Locate every Plasmodium falciparum-infected red blood cell.
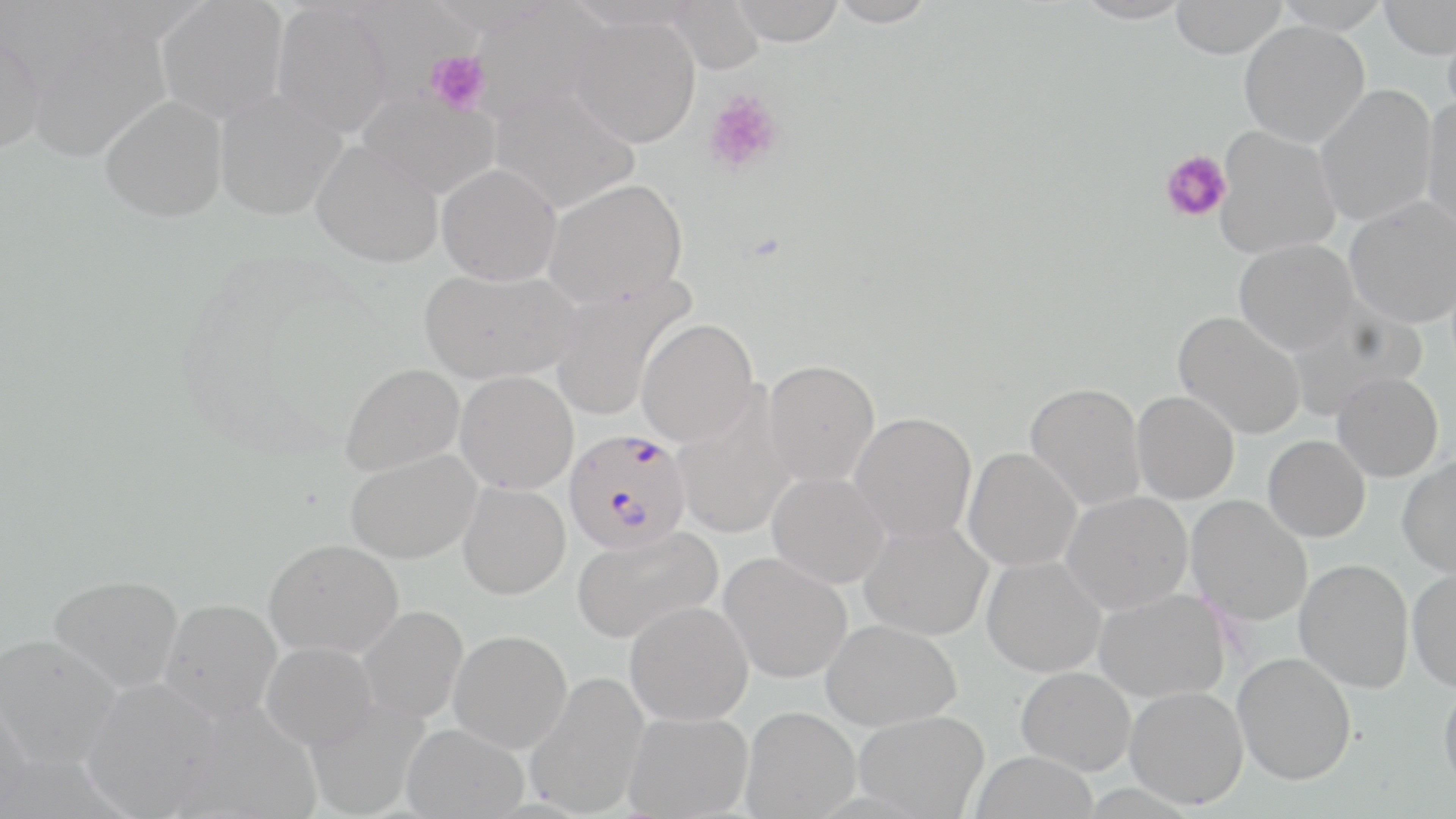

Approximate bounding boxes as (x1, y1, x2, y2) in pixels.
Plasmodium falciparum-infected red blood cells: (563, 428, 692, 553).

slide-level diagnosis = Plasmodium falciparum
preparation = thin blood film
stain = May-Grünwald-Giemsa
uninfected red blood cell locations = approximate bounding boxes as (x1, y1, x2, y2) in pixels: (156, 0, 289, 123), (666, 0, 765, 74), (728, 0, 845, 45), (826, 0, 939, 27), (1071, 0, 1194, 24), (1170, 0, 1288, 58), (1271, 0, 1392, 33), (1379, 1, 1456, 60), (271, 2, 394, 137), (469, 2, 607, 123), (568, 14, 701, 148), (1442, 14, 1456, 125), (24, 20, 170, 163), (1239, 21, 1370, 147), (0, 30, 46, 154), (1314, 85, 1438, 226), (489, 86, 641, 212), (213, 89, 346, 220), (357, 90, 500, 199), (99, 95, 227, 222), (1421, 98, 1456, 237), (1214, 126, 1341, 260), (311, 139, 443, 267), (436, 163, 563, 285), (543, 178, 688, 307), (1344, 197, 1456, 328), (1234, 238, 1359, 354), (419, 268, 579, 384), (550, 276, 695, 422), (1285, 299, 1427, 417), (1173, 311, 1306, 440), (636, 318, 758, 446), (763, 359, 880, 486), (340, 363, 464, 476), (455, 370, 579, 494), (1332, 371, 1443, 482), (1025, 382, 1146, 511), (671, 390, 796, 539), (1132, 391, 1239, 504), (849, 412, 977, 542), (1262, 435, 1370, 542), (964, 447, 1082, 571), (346, 449, 481, 564), (1397, 453, 1456, 578), (768, 471, 890, 588), (458, 481, 570, 599), (1062, 491, 1193, 613), (1186, 495, 1313, 626), (859, 520, 992, 640), (571, 525, 722, 644), (264, 539, 403, 658), (720, 552, 853, 683), (982, 556, 1106, 677), (1294, 559, 1414, 693), (1407, 567, 1456, 693), (48, 574, 184, 692), (1094, 588, 1230, 703), (160, 598, 281, 721), (625, 601, 753, 725), (357, 605, 469, 723), (821, 619, 962, 731), (449, 629, 572, 752), (0, 633, 122, 769), (262, 642, 377, 749), (1232, 652, 1357, 785), (1016, 666, 1136, 775), (525, 670, 650, 817), (81, 677, 222, 817), (1438, 679, 1456, 798), (1125, 686, 1249, 809), (0, 692, 33, 817), (304, 696, 431, 817), (741, 706, 861, 817), (853, 710, 989, 817), (623, 711, 753, 818), (402, 723, 528, 818), (969, 750, 1098, 819)
platelet locations = approximate bounding boxes as (x1, y1, x2, y2) in pixels: (426, 49, 490, 114), (701, 90, 785, 177), (1159, 150, 1232, 222)
magnification = 1000x
field of view = single
image size = 1456×819 pixels
modality = optical microscopy